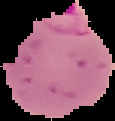

The area outside the segmented cell region is set to black. Malaria status: parasitized. Image is 115×121 pixels. From a thin blood film.